Report the malaria status of this cell.
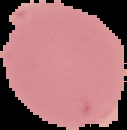

Uninfected.

Summary:
  - Preparation: thin blood smear
  - Image type: segmented cell region on a black background
  - Image size: 127×130 pixels